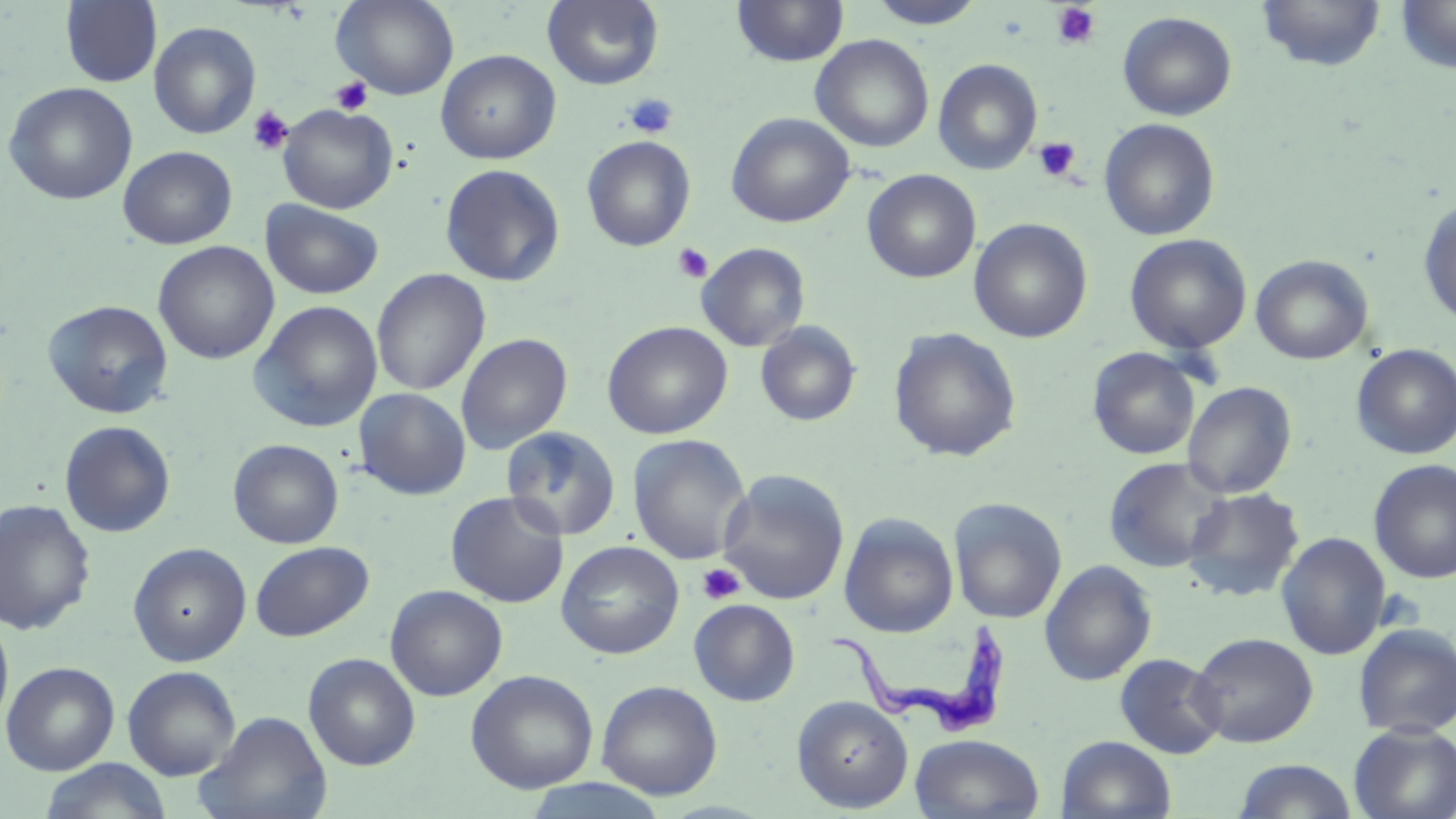
Summary:
  - Coordinate format: approximate bounding boxes as [x1, y1, x2, y2] in pixels
  - Platelet locations: [1051, 3, 1100, 49], [331, 77, 373, 115], [624, 93, 678, 138], [247, 105, 293, 156], [1034, 137, 1080, 182], [672, 243, 713, 283], [696, 562, 744, 605]
  - Uninfected red blood cell locations: [331, 0, 459, 101], [542, 0, 665, 90], [732, 0, 849, 67], [864, 0, 988, 29], [1256, 0, 1386, 73], [60, 1, 160, 87], [1394, 1, 1456, 74], [1117, 12, 1237, 121], [149, 21, 261, 139], [810, 34, 934, 153], [436, 49, 561, 164], [933, 59, 1043, 175], [2, 81, 138, 205], [278, 103, 398, 214], [726, 112, 854, 228], [1099, 118, 1220, 241], [582, 135, 696, 251], [118, 145, 237, 249], [440, 163, 565, 286], [862, 170, 981, 284], [1417, 197, 1456, 328], [261, 200, 384, 300], [970, 218, 1092, 343], [1125, 233, 1252, 354], [152, 241, 279, 365], [696, 243, 810, 352], [1250, 254, 1374, 365], [371, 269, 490, 396], [42, 299, 174, 418], [248, 300, 383, 433], [602, 321, 733, 439], [755, 321, 861, 427], [889, 327, 1022, 462], [456, 333, 572, 455], [1352, 343, 1456, 460], [1088, 347, 1201, 460], [1182, 381, 1297, 499], [353, 388, 471, 500], [59, 420, 176, 538], [501, 426, 622, 541], [627, 434, 752, 565], [228, 439, 344, 549], [1103, 456, 1231, 573], [1368, 459, 1456, 584], [716, 470, 850, 605], [1182, 487, 1305, 601], [445, 491, 569, 607], [949, 497, 1067, 624], [0, 499, 96, 635], [839, 513, 959, 638], [1276, 532, 1391, 660], [555, 540, 685, 659], [250, 541, 374, 641], [128, 542, 251, 667], [1040, 559, 1157, 686], [385, 584, 507, 701], [689, 599, 800, 706], [0, 613, 14, 731], [1353, 623, 1456, 738], [1188, 632, 1318, 747], [303, 652, 421, 770], [1114, 652, 1227, 759], [2, 661, 119, 775], [122, 665, 241, 781], [465, 669, 598, 793], [596, 680, 723, 800], [791, 695, 914, 812], [195, 710, 332, 819], [1349, 722, 1456, 819], [910, 733, 1045, 819], [1057, 735, 1176, 818], [40, 758, 171, 818], [1233, 759, 1359, 819], [517, 777, 673, 819]
  - Trypanosoma brucei locations: [826, 625, 1013, 740]
  - Slide-level diagnosis: Trypanosoma brucei
  - Image size: 1456×819 pixels
  - Modality: optical microscopy
  - Magnification: 1000x
  - Stain: May-Grünwald-Giemsa
  - Preparation: thin blood smear
  - Field of view: single